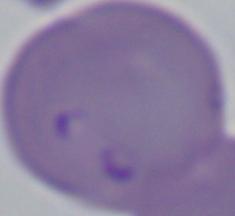
modality = photomicrograph
identification = Babesia
magnification = 1000x